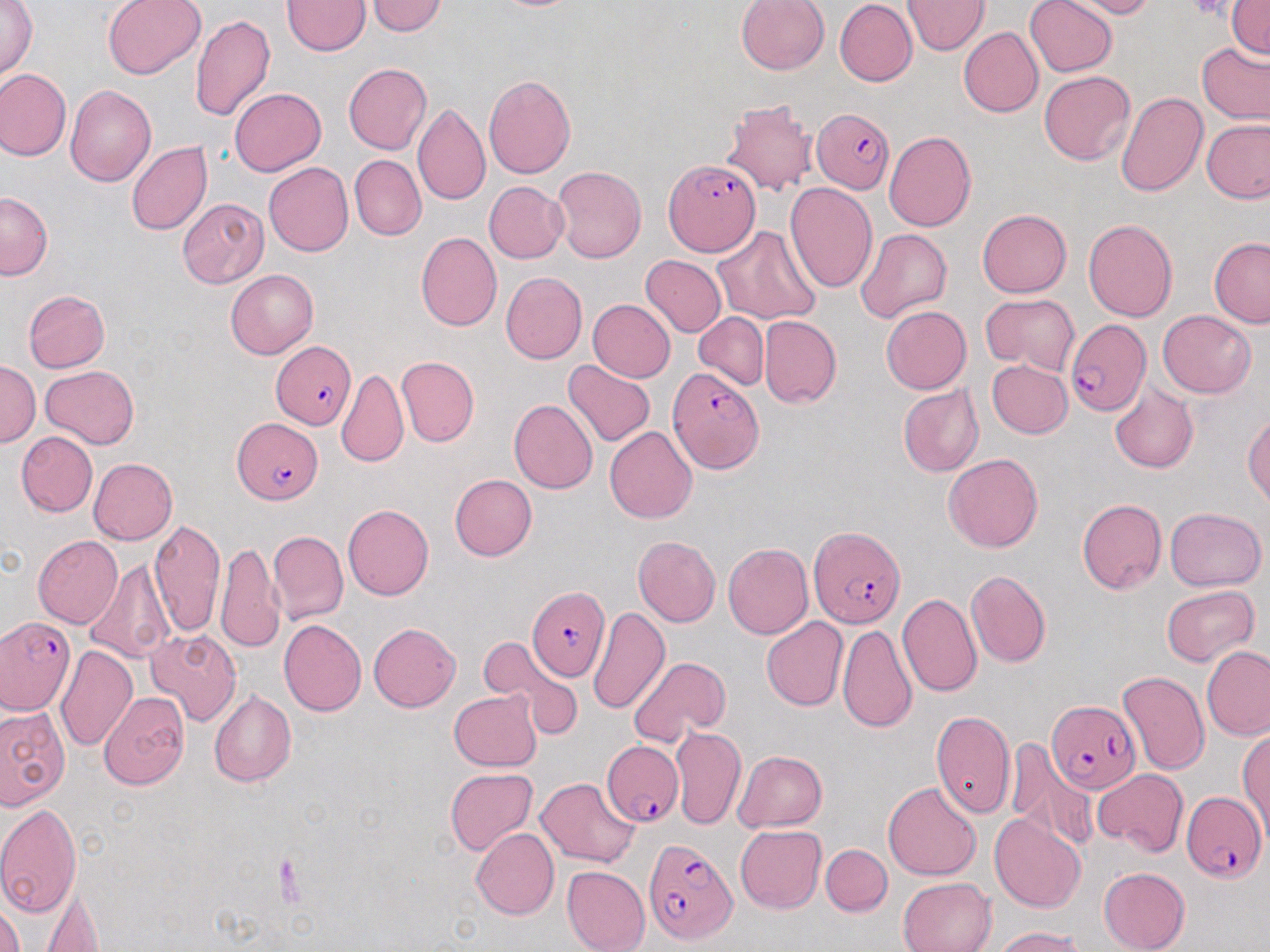
slide-level diagnosis = Plasmodium falciparum
magnification = 1000x
stain = May-Grünwald-Giemsa
field of view = single
uninfected red blood cell locations = approximate bounding boxes as named x1/y1/x2/y2 corners in pixels: (x1=1, y1=0, x2=37, y2=81), (x1=101, y1=0, x2=207, y2=81), (x1=736, y1=0, x2=829, y2=74), (x1=904, y1=0, x2=989, y2=55), (x1=1025, y1=0, x2=1118, y2=77), (x1=1059, y1=0, x2=1160, y2=19), (x1=283, y1=1, x2=369, y2=55), (x1=366, y1=1, x2=449, y2=36), (x1=835, y1=1, x2=917, y2=86), (x1=1228, y1=1, x2=1270, y2=59), (x1=190, y1=15, x2=274, y2=122), (x1=958, y1=26, x2=1043, y2=117), (x1=1197, y1=43, x2=1270, y2=125), (x1=343, y1=62, x2=431, y2=155), (x1=0, y1=69, x2=71, y2=161), (x1=1039, y1=70, x2=1136, y2=165), (x1=483, y1=74, x2=576, y2=180), (x1=65, y1=85, x2=158, y2=186), (x1=230, y1=87, x2=326, y2=176), (x1=1116, y1=92, x2=1208, y2=197), (x1=720, y1=97, x2=820, y2=196), (x1=413, y1=102, x2=490, y2=206), (x1=1202, y1=120, x2=1270, y2=202), (x1=884, y1=130, x2=977, y2=232), (x1=126, y1=142, x2=212, y2=235), (x1=349, y1=155, x2=425, y2=240), (x1=263, y1=162, x2=353, y2=257), (x1=552, y1=165, x2=646, y2=264), (x1=484, y1=181, x2=569, y2=262), (x1=785, y1=182, x2=877, y2=292), (x1=0, y1=191, x2=52, y2=280), (x1=177, y1=199, x2=268, y2=287), (x1=977, y1=209, x2=1072, y2=297), (x1=1083, y1=218, x2=1178, y2=322), (x1=715, y1=225, x2=820, y2=325), (x1=854, y1=228, x2=952, y2=324), (x1=415, y1=231, x2=502, y2=331), (x1=1209, y1=238, x2=1270, y2=327), (x1=641, y1=256, x2=727, y2=337), (x1=226, y1=269, x2=319, y2=358), (x1=500, y1=271, x2=587, y2=363), (x1=23, y1=290, x2=110, y2=372), (x1=33, y1=290, x2=123, y2=451), (x1=981, y1=293, x2=1080, y2=375), (x1=588, y1=300, x2=675, y2=382), (x1=881, y1=305, x2=971, y2=393), (x1=1157, y1=310, x2=1257, y2=397), (x1=694, y1=312, x2=768, y2=389), (x1=759, y1=314, x2=841, y2=408), (x1=395, y1=356, x2=479, y2=447), (x1=562, y1=359, x2=656, y2=446), (x1=987, y1=361, x2=1072, y2=439), (x1=1, y1=362, x2=40, y2=447), (x1=40, y1=365, x2=139, y2=449), (x1=338, y1=368, x2=409, y2=468), (x1=1109, y1=382, x2=1199, y2=473), (x1=897, y1=384, x2=983, y2=478), (x1=509, y1=398, x2=598, y2=494), (x1=1243, y1=412, x2=1270, y2=507), (x1=604, y1=426, x2=697, y2=524), (x1=16, y1=431, x2=97, y2=516), (x1=943, y1=453, x2=1043, y2=553), (x1=88, y1=458, x2=177, y2=544), (x1=449, y1=474, x2=537, y2=561), (x1=1076, y1=498, x2=1166, y2=594), (x1=343, y1=504, x2=434, y2=600), (x1=1165, y1=506, x2=1266, y2=591), (x1=148, y1=518, x2=224, y2=638), (x1=268, y1=530, x2=347, y2=625), (x1=32, y1=535, x2=124, y2=629), (x1=633, y1=535, x2=721, y2=626), (x1=215, y1=542, x2=283, y2=654), (x1=722, y1=543, x2=812, y2=639), (x1=83, y1=559, x2=175, y2=664), (x1=965, y1=569, x2=1051, y2=669), (x1=1161, y1=586, x2=1258, y2=667), (x1=898, y1=593, x2=982, y2=697), (x1=588, y1=606, x2=670, y2=716), (x1=854, y1=608, x2=976, y2=720), (x1=761, y1=617, x2=848, y2=711), (x1=279, y1=619, x2=366, y2=717), (x1=367, y1=622, x2=460, y2=711), (x1=837, y1=624, x2=917, y2=734), (x1=144, y1=628, x2=243, y2=727), (x1=479, y1=636, x2=583, y2=739), (x1=55, y1=644, x2=138, y2=752), (x1=1201, y1=646, x2=1269, y2=740), (x1=628, y1=655, x2=731, y2=746), (x1=1118, y1=672, x2=1209, y2=775), (x1=208, y1=690, x2=296, y2=787), (x1=449, y1=690, x2=542, y2=770), (x1=99, y1=691, x2=189, y2=790), (x1=0, y1=704, x2=68, y2=808), (x1=930, y1=710, x2=1015, y2=819), (x1=670, y1=726, x2=746, y2=830), (x1=1237, y1=727, x2=1270, y2=835), (x1=1005, y1=743, x2=1100, y2=855), (x1=733, y1=750, x2=827, y2=831), (x1=445, y1=767, x2=537, y2=855), (x1=1093, y1=769, x2=1188, y2=857), (x1=535, y1=777, x2=641, y2=868), (x1=883, y1=781, x2=982, y2=880), (x1=0, y1=803, x2=81, y2=919), (x1=990, y1=812, x2=1086, y2=913), (x1=735, y1=825, x2=826, y2=914), (x1=470, y1=828, x2=559, y2=920), (x1=821, y1=844, x2=892, y2=916), (x1=562, y1=866, x2=650, y2=952), (x1=1099, y1=867, x2=1191, y2=952), (x1=898, y1=877, x2=997, y2=951), (x1=39, y1=884, x2=105, y2=951), (x1=0, y1=902, x2=25, y2=952), (x1=991, y1=926, x2=1087, y2=952)
Plasmodium falciparum-infected red blood cell locations = approximate bounding boxes as named x1/y1/x2/y2 corners in pixels: (x1=813, y1=107, x2=895, y2=193), (x1=663, y1=159, x2=760, y2=256), (x1=1064, y1=318, x2=1150, y2=416), (x1=271, y1=341, x2=357, y2=430), (x1=667, y1=367, x2=762, y2=473), (x1=233, y1=417, x2=323, y2=504), (x1=810, y1=527, x2=907, y2=630), (x1=527, y1=585, x2=610, y2=678), (x1=0, y1=616, x2=74, y2=717), (x1=1046, y1=699, x2=1141, y2=792), (x1=601, y1=740, x2=685, y2=826), (x1=1181, y1=790, x2=1266, y2=884), (x1=644, y1=837, x2=736, y2=943)
preparation = thin blood smear
image size = 1270×952 pixels
modality = optical microscopy